Assess this cell for malaria.
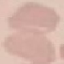
Uninfected.

Acquired by smartphone through the microscope eyepiece. Thin blood smear. Cell patch, automatically extracted from a larger field of view and resized to 64 × 64 pixels. Giemsa-stained preparation.